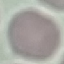
malaria status = uninfected
image type = automatically extracted cell patch, resized to 64 × 64 pixels
preparation = thin blood smear
stain = Giemsa
capture = smartphone through the microscope eyepiece